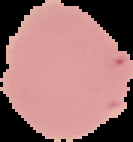

From a thin blood film. The area outside the segmented cell region is set to black. Malaria status: uninfected. Image is 133×142 pixels.